Classify this cell by malaria status.
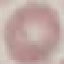
It is uninfected.

Giemsa stain. Photographed with a smartphone camera at the microscope eyepiece. Thin blood smear. Cell patch, automatically extracted from a larger field of view and resized to 64 × 64 pixels.